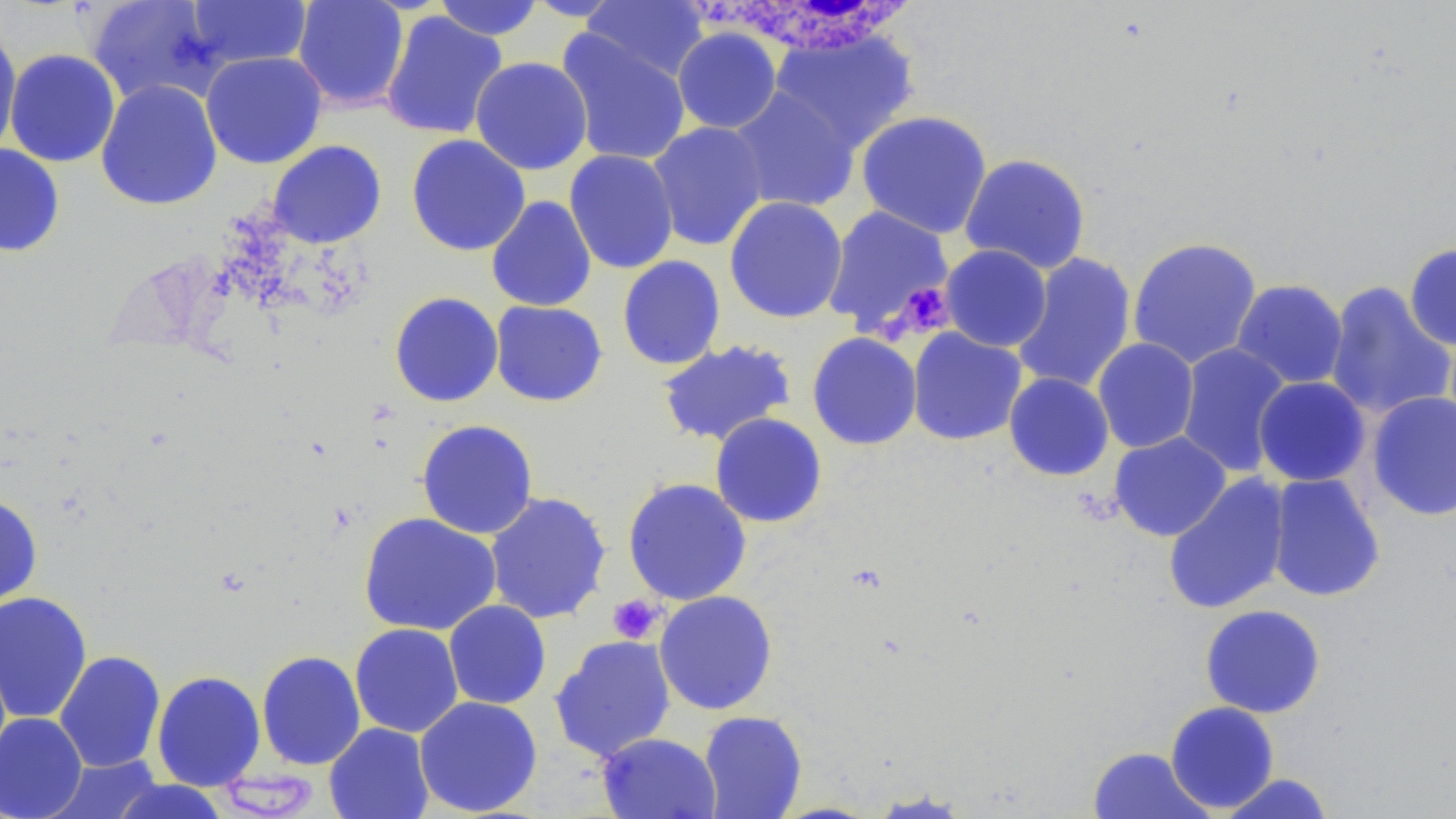

Summary:
  - Coordinate format: approximate bounding boxes as named x1/y1/x2/y2 corners in pixels
  - White blood cell locations: (x1=700, y1=3, x2=924, y2=58)
  - Uninfected red blood cell locations: (x1=85, y1=0, x2=226, y2=107), (x1=292, y1=0, x2=410, y2=112), (x1=431, y1=0, x2=546, y2=41), (x1=581, y1=0, x2=710, y2=83), (x1=186, y1=1, x2=311, y2=70), (x1=380, y1=11, x2=508, y2=140), (x1=0, y1=25, x2=22, y2=158), (x1=672, y1=27, x2=782, y2=134), (x1=770, y1=28, x2=919, y2=153), (x1=556, y1=30, x2=692, y2=167), (x1=5, y1=49, x2=121, y2=168), (x1=200, y1=51, x2=327, y2=169), (x1=470, y1=56, x2=593, y2=175), (x1=95, y1=79, x2=223, y2=211), (x1=727, y1=86, x2=861, y2=214), (x1=855, y1=110, x2=993, y2=238), (x1=647, y1=121, x2=769, y2=252), (x1=406, y1=134, x2=531, y2=256), (x1=266, y1=140, x2=387, y2=249), (x1=0, y1=143, x2=65, y2=257), (x1=564, y1=149, x2=679, y2=274), (x1=959, y1=153, x2=1091, y2=274), (x1=486, y1=195, x2=597, y2=312), (x1=724, y1=196, x2=848, y2=324), (x1=821, y1=205, x2=954, y2=337), (x1=1127, y1=236, x2=1263, y2=369), (x1=1404, y1=243, x2=1456, y2=351), (x1=939, y1=244, x2=1052, y2=352), (x1=1011, y1=253, x2=1137, y2=394), (x1=617, y1=255, x2=726, y2=371), (x1=1231, y1=279, x2=1348, y2=388), (x1=1325, y1=281, x2=1454, y2=419), (x1=389, y1=291, x2=503, y2=407), (x1=489, y1=300, x2=607, y2=406), (x1=906, y1=327, x2=1028, y2=446), (x1=807, y1=332, x2=922, y2=450), (x1=1092, y1=338, x2=1199, y2=453), (x1=656, y1=339, x2=798, y2=447), (x1=1176, y1=342, x2=1293, y2=478), (x1=1004, y1=372, x2=1114, y2=481), (x1=1253, y1=376, x2=1371, y2=487), (x1=1366, y1=391, x2=1456, y2=521), (x1=709, y1=412, x2=827, y2=528), (x1=415, y1=419, x2=539, y2=539), (x1=1109, y1=431, x2=1232, y2=541), (x1=1265, y1=472, x2=1385, y2=602), (x1=1162, y1=473, x2=1291, y2=615), (x1=622, y1=477, x2=752, y2=605), (x1=485, y1=491, x2=612, y2=625), (x1=0, y1=494, x2=43, y2=608), (x1=358, y1=512, x2=501, y2=636), (x1=653, y1=590, x2=778, y2=715), (x1=0, y1=591, x2=93, y2=724), (x1=443, y1=600, x2=552, y2=710), (x1=1200, y1=604, x2=1326, y2=719), (x1=349, y1=623, x2=464, y2=738), (x1=549, y1=634, x2=677, y2=762), (x1=54, y1=650, x2=166, y2=773), (x1=256, y1=650, x2=366, y2=770), (x1=151, y1=670, x2=266, y2=791), (x1=414, y1=695, x2=543, y2=817), (x1=1165, y1=701, x2=1280, y2=813), (x1=697, y1=710, x2=807, y2=819), (x1=0, y1=711, x2=88, y2=819), (x1=324, y1=722, x2=435, y2=819), (x1=597, y1=732, x2=721, y2=819), (x1=1088, y1=746, x2=1214, y2=819), (x1=46, y1=755, x2=162, y2=818), (x1=1218, y1=773, x2=1335, y2=818), (x1=109, y1=779, x2=231, y2=819), (x1=865, y1=790, x2=976, y2=818)
  - Platelet locations: (x1=891, y1=281, x2=955, y2=339), (x1=608, y1=594, x2=665, y2=645)
  - Slide-level diagnosis: negative for blood parasites
  - Magnification: 1000x
  - Modality: light microscopy
  - Image size: 1456×819 pixels
  - Stain: May-Grünwald-Giemsa
  - Field of view: one of a larger specimen
  - Preparation: thin blood film